Report the malaria status of this cell.
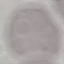
Uninfected.

Summary:
  - Capture: smartphone through the microscope eyepiece
  - Image type: automatically extracted cell patch, resized to 64 × 64 pixels
  - Stain: Giemsa
  - Preparation: thin blood smear